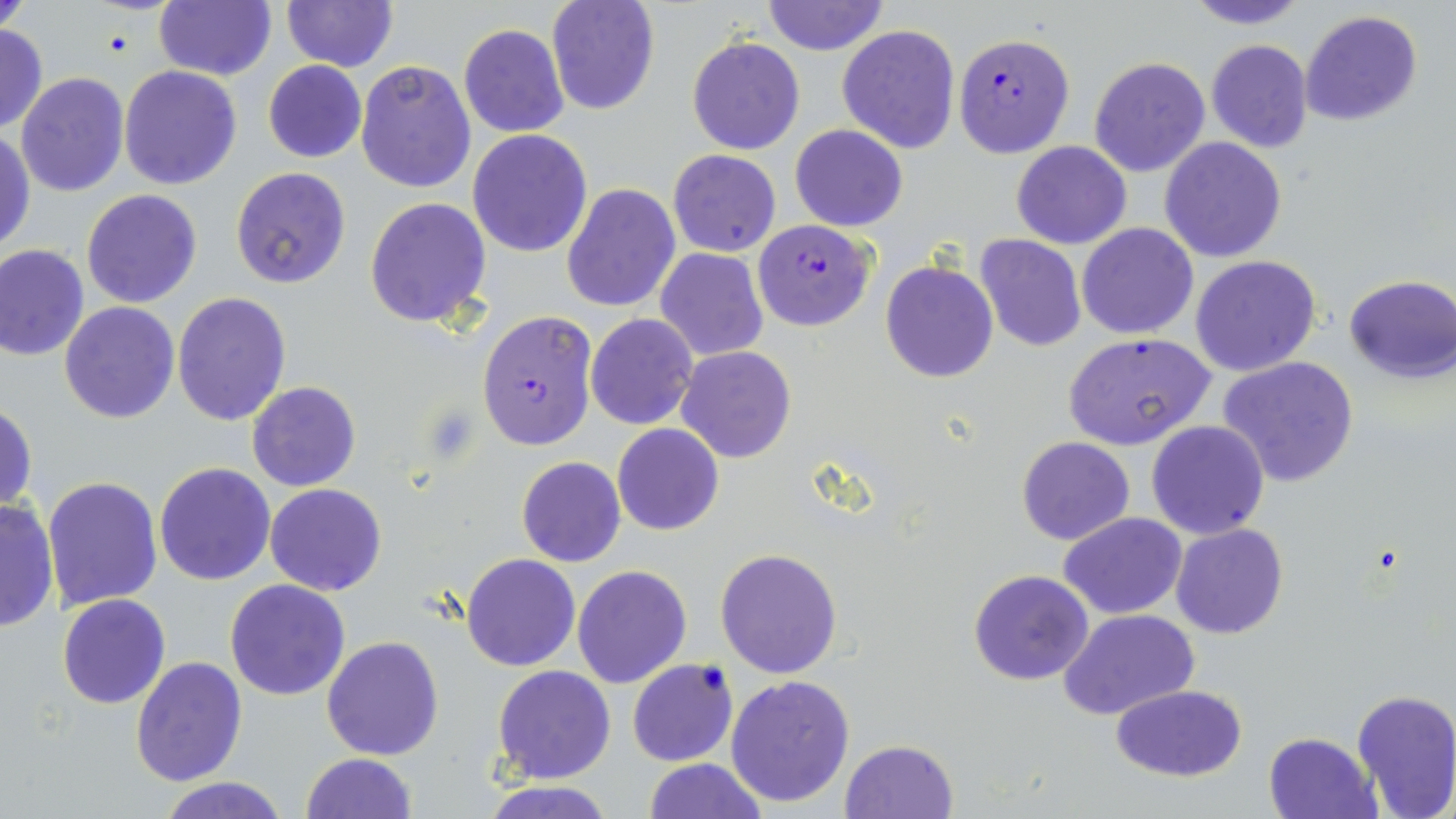

Summary:
  - Coordinate format: approximate bounding boxes as named x1/y1/x2/y2 corners in pixels
  - Uninfected red blood cell locations: (x1=0, y1=0, x2=34, y2=35), (x1=153, y1=0, x2=274, y2=80), (x1=545, y1=0, x2=660, y2=115), (x1=761, y1=0, x2=889, y2=56), (x1=1181, y1=0, x2=1312, y2=29), (x1=282, y1=1, x2=398, y2=72), (x1=1300, y1=11, x2=1423, y2=127), (x1=0, y1=21, x2=48, y2=137), (x1=458, y1=24, x2=571, y2=138), (x1=837, y1=24, x2=960, y2=154), (x1=687, y1=35, x2=806, y2=156), (x1=1206, y1=39, x2=1314, y2=155), (x1=1088, y1=57, x2=1211, y2=178), (x1=355, y1=59, x2=476, y2=195), (x1=262, y1=60, x2=367, y2=163), (x1=117, y1=65, x2=242, y2=190), (x1=15, y1=71, x2=130, y2=196), (x1=790, y1=124, x2=908, y2=231), (x1=0, y1=127, x2=36, y2=256), (x1=467, y1=128, x2=593, y2=257), (x1=1160, y1=137, x2=1288, y2=262), (x1=1012, y1=140, x2=1131, y2=249), (x1=667, y1=149, x2=782, y2=258), (x1=230, y1=166, x2=353, y2=287), (x1=561, y1=182, x2=681, y2=313), (x1=72, y1=188, x2=192, y2=425), (x1=80, y1=189, x2=203, y2=309), (x1=365, y1=197, x2=492, y2=329), (x1=1077, y1=222, x2=1199, y2=339), (x1=974, y1=234, x2=1086, y2=351), (x1=0, y1=245, x2=90, y2=362), (x1=655, y1=248, x2=769, y2=360), (x1=1190, y1=254, x2=1322, y2=377), (x1=880, y1=261, x2=999, y2=383), (x1=1342, y1=275, x2=1454, y2=383), (x1=171, y1=293, x2=292, y2=426), (x1=59, y1=301, x2=181, y2=423), (x1=585, y1=313, x2=698, y2=430), (x1=1063, y1=332, x2=1215, y2=450), (x1=676, y1=346, x2=797, y2=463), (x1=1217, y1=356, x2=1359, y2=487), (x1=247, y1=381, x2=361, y2=491), (x1=1, y1=400, x2=37, y2=514), (x1=1146, y1=419, x2=1270, y2=539), (x1=612, y1=423, x2=724, y2=535), (x1=1016, y1=436, x2=1136, y2=546), (x1=516, y1=456, x2=626, y2=567), (x1=153, y1=462, x2=276, y2=586), (x1=42, y1=476, x2=163, y2=610), (x1=265, y1=483, x2=387, y2=596), (x1=0, y1=496, x2=59, y2=635), (x1=1059, y1=512, x2=1186, y2=619), (x1=1171, y1=522, x2=1288, y2=639), (x1=715, y1=549, x2=844, y2=678), (x1=469, y1=551, x2=591, y2=782), (x1=461, y1=554, x2=580, y2=672), (x1=572, y1=565, x2=691, y2=688), (x1=968, y1=569, x2=1095, y2=686), (x1=224, y1=579, x2=350, y2=701), (x1=57, y1=594, x2=169, y2=709), (x1=1058, y1=608, x2=1198, y2=719), (x1=321, y1=635, x2=446, y2=759), (x1=131, y1=657, x2=247, y2=787), (x1=627, y1=660, x2=739, y2=766), (x1=492, y1=665, x2=616, y2=784), (x1=724, y1=675, x2=856, y2=808), (x1=1109, y1=685, x2=1249, y2=781), (x1=1351, y1=688, x2=1456, y2=818), (x1=1263, y1=732, x2=1381, y2=819), (x1=841, y1=739, x2=959, y2=818), (x1=300, y1=752, x2=417, y2=818), (x1=642, y1=758, x2=768, y2=818), (x1=159, y1=776, x2=292, y2=819), (x1=472, y1=779, x2=623, y2=818)
  - Plasmodium falciparum-infected red blood cell locations: (x1=953, y1=31, x2=1075, y2=157), (x1=753, y1=220, x2=876, y2=331), (x1=475, y1=309, x2=598, y2=450)
  - Slide-level diagnosis: Plasmodium falciparum
  - Modality: optical microscopy
  - Preparation: thin blood smear
  - Image size: 1456×819 pixels
  - Magnification: 1000x
  - Field of view: single
  - Stain: May-Grünwald-Giemsa